Classify this cell by malaria status.
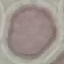

It is uninfected.

Summary:
  - Stain: Giemsa
  - Capture: smartphone camera at the microscope eyepiece
  - Image type: cell patch, automatically extracted from a larger field of view and resized to 64 × 64 pixels
  - Preparation: thin blood film